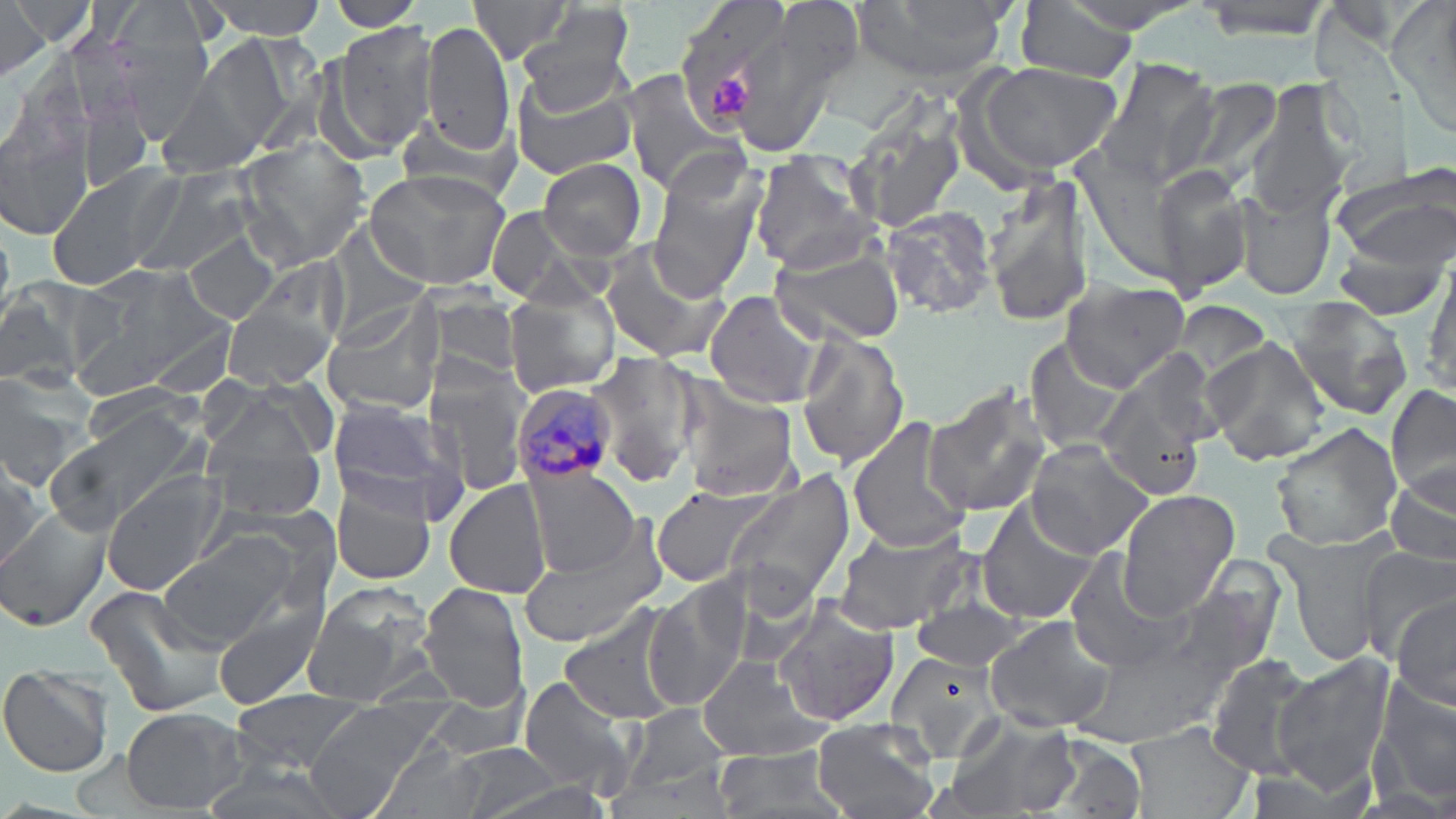

Summary:
  - Coordinate format: approximate bounding boxes as (x1, y1, x2, y2) in pixels
  - Platelet locations: (711, 75, 756, 119)
  - Uninfected red blood cell locations: (1, 0, 88, 58), (199, 0, 330, 38), (326, 0, 425, 31), (677, 0, 796, 126), (698, 0, 858, 159), (852, 0, 1015, 88), (1194, 0, 1337, 41), (463, 1, 583, 65), (1013, 1, 1141, 82), (0, 3, 50, 84), (1389, 4, 1456, 137), (518, 10, 634, 110), (108, 15, 215, 137), (420, 21, 514, 152), (333, 24, 437, 149), (170, 35, 295, 169), (968, 59, 1125, 180), (1092, 59, 1223, 190), (617, 71, 743, 193), (509, 73, 639, 179), (1169, 76, 1285, 194), (1247, 79, 1354, 217), (74, 92, 153, 194), (840, 107, 968, 235), (0, 110, 95, 239), (395, 115, 516, 207), (235, 139, 371, 271), (748, 151, 880, 274), (538, 157, 649, 261), (44, 160, 188, 288), (1331, 161, 1456, 267), (646, 163, 763, 302), (1151, 167, 1256, 298), (364, 168, 513, 290), (130, 170, 252, 279), (982, 172, 1093, 328), (1235, 183, 1338, 300), (481, 206, 598, 305), (880, 207, 997, 320), (324, 221, 430, 337), (182, 234, 280, 325), (767, 238, 906, 344), (594, 244, 732, 365), (1328, 252, 1451, 321), (251, 256, 351, 351), (1426, 263, 1456, 397), (1061, 277, 1192, 390), (0, 281, 99, 393), (421, 289, 525, 383), (505, 289, 620, 397), (702, 290, 827, 408), (319, 298, 444, 420), (1288, 298, 1416, 420), (222, 300, 335, 392), (1175, 301, 1274, 391), (140, 314, 236, 400), (794, 331, 911, 470), (1024, 336, 1134, 457), (1201, 339, 1331, 467), (589, 352, 699, 487), (1094, 362, 1215, 502), (425, 365, 533, 492), (0, 366, 100, 488), (678, 376, 800, 500), (1386, 382, 1455, 505), (922, 384, 1056, 518), (79, 385, 199, 453), (205, 386, 326, 467), (323, 400, 471, 520), (46, 406, 206, 531), (848, 418, 974, 553), (1269, 422, 1403, 551), (202, 423, 329, 523), (1025, 441, 1155, 557), (0, 450, 50, 569), (522, 464, 640, 579), (1385, 465, 1456, 572), (725, 467, 857, 610), (102, 474, 229, 596), (329, 476, 438, 587), (445, 478, 548, 600), (648, 484, 775, 588), (1117, 490, 1240, 614), (976, 503, 1102, 625), (0, 507, 109, 630), (830, 521, 973, 633), (516, 524, 665, 649), (1269, 527, 1397, 665), (158, 534, 298, 648), (1352, 547, 1455, 661), (1062, 549, 1196, 675), (1170, 564, 1283, 686), (644, 581, 749, 711), (300, 582, 435, 705), (419, 582, 531, 709), (84, 583, 235, 723), (908, 597, 1029, 670), (1390, 597, 1454, 711), (773, 602, 902, 727), (212, 603, 327, 711), (558, 606, 687, 728), (984, 615, 1117, 732), (1073, 630, 1239, 745), (882, 651, 1007, 765), (1270, 654, 1394, 794), (1203, 655, 1317, 777), (695, 656, 835, 762), (0, 666, 115, 778), (517, 675, 638, 796), (1371, 675, 1456, 806), (413, 693, 536, 758), (226, 694, 369, 773), (303, 705, 436, 818), (626, 705, 732, 795), (121, 707, 249, 814), (808, 715, 942, 819), (943, 715, 1078, 819), (1125, 722, 1255, 819), (1037, 732, 1151, 819), (372, 742, 493, 819), (446, 743, 568, 819), (708, 744, 849, 819), (194, 758, 344, 819)
  - Plasmodium malariae-infected red blood cell locations: (513, 381, 617, 487)
  - Slide-level diagnosis: Plasmodium malariae
  - Field of view: single
  - Image size: 1456×819 pixels
  - Preparation: thin blood smear
  - Stain: May-Grünwald-Giemsa
  - Magnification: 1000x
  - Modality: light microscopy